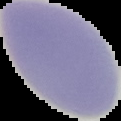

{
  "result": "no Plasmodium parasites seen",
  "image_type": "segmented cell region on a black background",
  "preparation": "thin blood film",
  "image_size": "121×121 pixels"
}